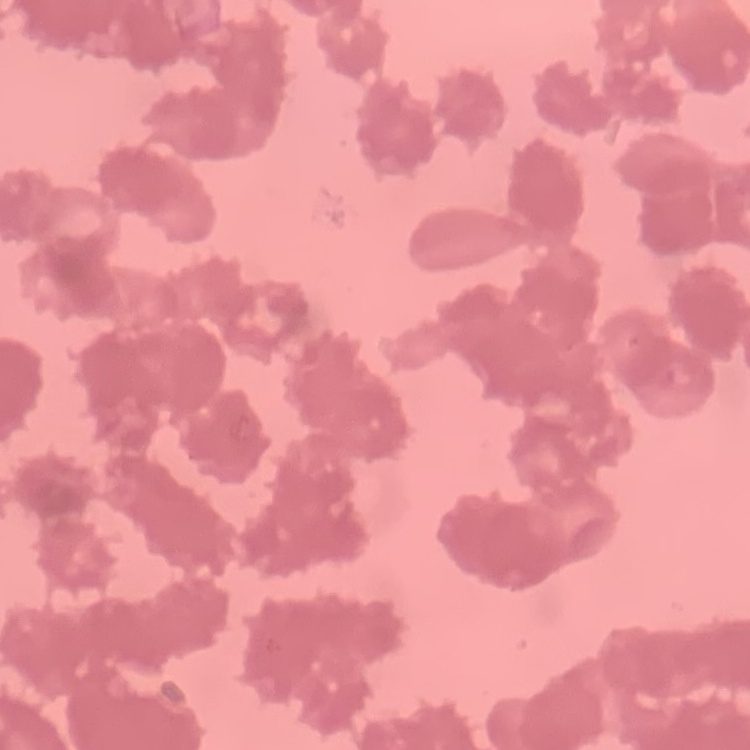
{
  "red_blood_cell_morphology": "rouleaux formation",
  "image_type": "one tile cut from a larger photomicrograph",
  "stain": "Field's or Giemsa",
  "preparation": "thin blood film"
}